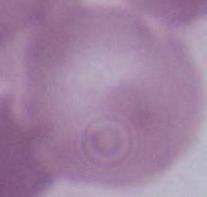

Summary:
  - Magnification: 1000x
  - Identification: erythrocyte
  - Modality: photomicrograph